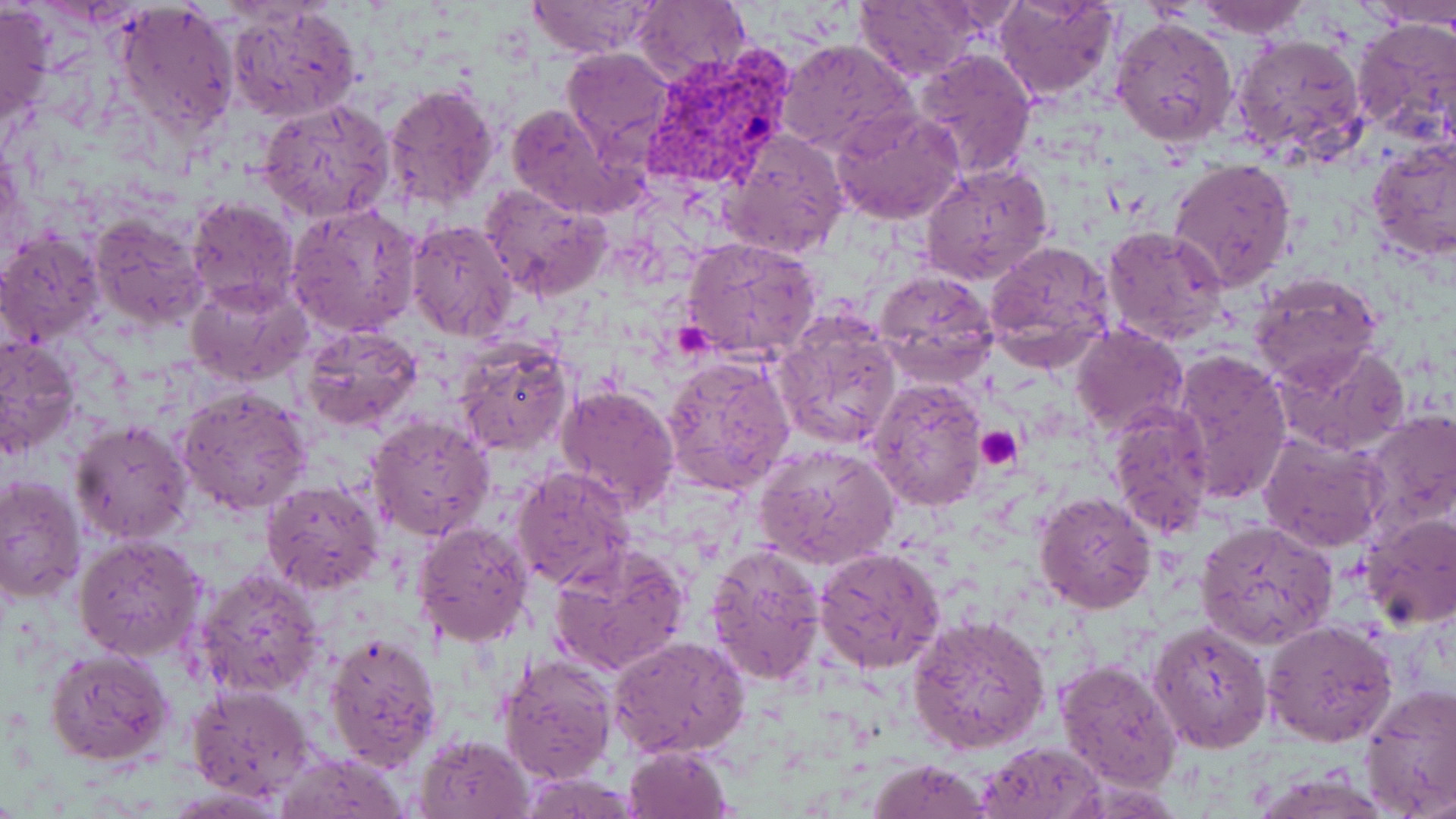
Summary:
  - Coordinate format: approximate bounding boxes as (x1, y1, x2, y2) in pixels
  - Plasmodium vivax-infected red blood cell locations: (645, 50, 792, 192)
  - Platelet locations: (974, 426, 1022, 470)
  - Uninfected red blood cell locations: (0, 0, 55, 133), (525, 0, 662, 58), (996, 0, 1120, 100), (1194, 0, 1309, 40), (628, 1, 751, 85), (854, 1, 979, 83), (1362, 1, 1456, 30), (114, 3, 239, 140), (226, 3, 361, 123), (1110, 15, 1238, 149), (1351, 16, 1456, 147), (1229, 31, 1366, 163), (777, 38, 913, 154), (561, 47, 672, 154), (912, 49, 1037, 180), (383, 83, 500, 214), (256, 98, 397, 226), (506, 102, 630, 218), (830, 108, 965, 223), (722, 129, 850, 261), (1366, 141, 1455, 260), (1166, 156, 1298, 293), (920, 163, 1055, 284), (479, 182, 610, 300), (186, 197, 299, 311), (288, 203, 423, 337), (89, 213, 210, 332), (405, 218, 518, 340), (1102, 225, 1229, 344), (0, 231, 106, 346), (682, 237, 824, 363), (983, 240, 1117, 369), (873, 270, 999, 384), (1248, 271, 1382, 388), (186, 280, 311, 385), (774, 311, 902, 452), (1070, 324, 1189, 438), (301, 325, 422, 433), (0, 334, 82, 459), (455, 341, 576, 458), (1271, 343, 1411, 456), (1168, 350, 1292, 505), (662, 356, 795, 494), (867, 378, 991, 513), (554, 384, 680, 515), (175, 386, 313, 517), (1106, 403, 1215, 540), (1361, 410, 1456, 536), (366, 415, 494, 539), (70, 420, 194, 545), (1257, 432, 1390, 552), (753, 443, 898, 570), (513, 466, 635, 588), (0, 475, 86, 607), (260, 480, 385, 598), (1034, 490, 1156, 613), (1360, 512, 1456, 630), (1195, 519, 1338, 648), (413, 520, 534, 648), (74, 535, 205, 661), (705, 546, 829, 689), (815, 546, 947, 675), (550, 547, 689, 676), (194, 564, 326, 699), (907, 615, 1051, 755), (1262, 620, 1398, 746), (1148, 623, 1273, 753), (323, 631, 444, 771), (610, 635, 749, 759), (45, 647, 174, 766), (498, 655, 617, 786), (1055, 658, 1183, 793), (185, 685, 314, 799), (1360, 686, 1456, 815), (415, 731, 536, 819), (978, 740, 1107, 819), (623, 745, 733, 819), (277, 753, 410, 818), (865, 758, 993, 819)
  - Slide-level diagnosis: Plasmodium vivax
  - Preparation: thin blood smear
  - Modality: light microscopy
  - Field of view: one of a larger specimen
  - Magnification: 1000x
  - Stain: May-Grünwald-Giemsa
  - Image size: 1456×819 pixels